State which parasite is depicted.
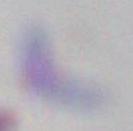
This is Toxoplasma gondii.

Captured at 1000x magnification. Micrograph.